Outline each blood parasite and name the species.
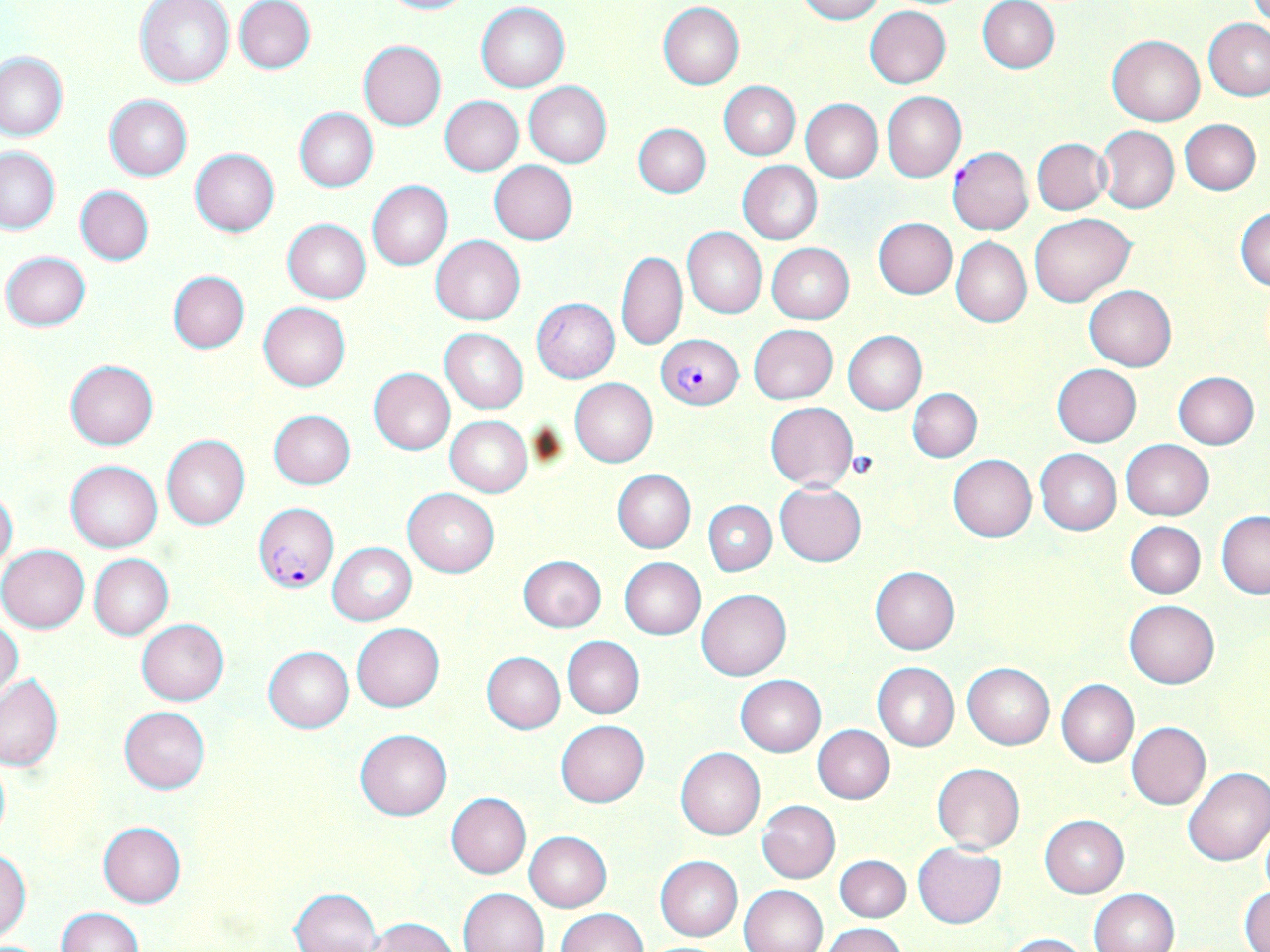

Approximate bounding boxes as (x1, y1, x2, y2) in pixels.
Plasmodium falciparum-infected red blood cells: (655, 333, 744, 409), (254, 504, 338, 591).
No Plasmodium ovale, Plasmodium malariae, Plasmodium vivax, Babesia divergens, or Trypanosoma brucei observed.

slide-level diagnosis = Plasmodium falciparum
platelet locations = approximate bounding boxes as (x1, y1, x2, y2) in pixels: (847, 450, 879, 479)
field of view = single
stain = May-Grünwald-Giemsa
preparation = thin blood film
magnification = 1000x
modality = optical microscopy
image size = 1270×952 pixels
uninfected red blood cell locations = approximate bounding boxes as (x1, y1, x2, y2) in pixels: (135, 0, 235, 88), (374, 0, 475, 15), (794, 0, 884, 23), (233, 1, 315, 74), (978, 1, 1061, 74), (658, 2, 745, 88), (476, 3, 570, 92), (864, 5, 951, 88), (1203, 18, 1270, 101), (1107, 35, 1205, 126), (358, 40, 446, 130), (0, 50, 68, 142), (524, 81, 612, 167), (718, 81, 800, 160), (882, 91, 966, 183), (103, 94, 192, 181), (439, 95, 524, 175), (800, 98, 883, 182), (295, 108, 378, 192), (1180, 119, 1260, 195), (633, 123, 711, 198), (1096, 126, 1179, 214), (1032, 138, 1111, 214), (0, 147, 60, 234), (947, 147, 1033, 235), (190, 148, 280, 235), (489, 160, 577, 245), (737, 161, 823, 244), (367, 180, 453, 271), (75, 186, 154, 266), (1234, 205, 1270, 292), (1030, 213, 1136, 307), (873, 217, 957, 299), (282, 218, 371, 303), (682, 228, 767, 319), (431, 235, 526, 325), (951, 237, 1032, 327), (767, 243, 855, 323), (2, 250, 91, 332), (615, 251, 687, 352), (169, 271, 249, 353), (1085, 285, 1176, 371), (531, 298, 620, 383), (259, 302, 351, 391), (749, 324, 838, 404), (440, 328, 527, 413), (843, 331, 927, 414), (64, 360, 159, 450), (1051, 364, 1142, 447), (368, 368, 456, 454), (1172, 371, 1259, 448), (570, 378, 658, 467), (908, 388, 982, 461), (766, 402, 858, 490), (268, 409, 356, 489), (445, 416, 533, 496), (161, 434, 251, 530), (1120, 439, 1215, 521), (1035, 449, 1121, 534), (948, 454, 1037, 542), (65, 461, 162, 553), (612, 469, 695, 552), (776, 482, 866, 566), (0, 488, 18, 573), (403, 488, 499, 576), (703, 500, 775, 575), (1217, 512, 1270, 598), (1124, 521, 1205, 598), (328, 543, 416, 625), (0, 544, 90, 632), (89, 554, 173, 640), (516, 554, 607, 632), (618, 558, 706, 640), (869, 566, 960, 654), (696, 589, 791, 680), (1124, 600, 1219, 689), (136, 619, 229, 705), (0, 621, 23, 704), (351, 623, 444, 711), (562, 637, 645, 718), (263, 646, 354, 733), (481, 652, 565, 733), (872, 662, 960, 752), (963, 662, 1054, 749), (0, 674, 62, 771), (735, 675, 826, 756), (1057, 679, 1139, 767), (120, 706, 210, 794), (555, 721, 649, 805), (1126, 722, 1211, 811), (812, 725, 893, 804), (354, 729, 452, 820), (675, 746, 765, 840), (0, 753, 10, 848), (931, 762, 1026, 853), (1182, 767, 1270, 867), (445, 793, 531, 878), (757, 800, 841, 883), (1041, 815, 1128, 898), (98, 822, 186, 908), (1259, 824, 1270, 896), (524, 831, 611, 912), (914, 843, 1005, 927), (0, 850, 32, 939), (835, 854, 912, 921), (655, 855, 742, 941), (738, 884, 827, 952), (1239, 885, 1270, 951), (291, 887, 381, 952), (458, 887, 549, 952), (1088, 888, 1178, 952), (56, 907, 142, 952), (555, 908, 647, 952), (366, 918, 459, 952), (823, 923, 907, 952), (999, 931, 1090, 951)